State which parasite is depicted.
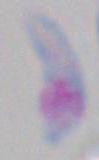
This is Toxoplasma gondii.

modality: photomicrograph
magnification: 1000x